Assess the morphology of the erythrocytes.
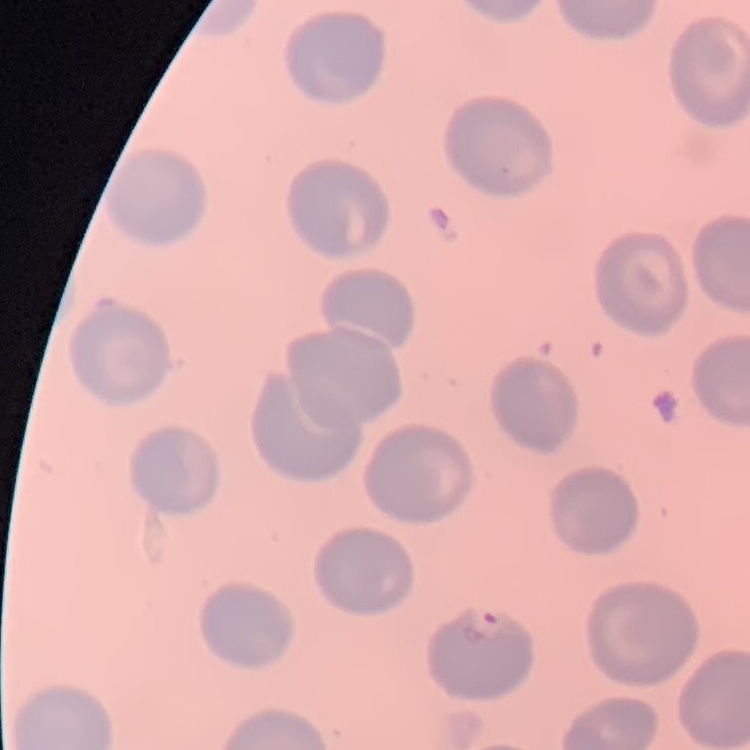

No rouleaux formation.

Stained with either Field's or Giemsa. Thin blood smear. One tile cut from a larger photomicrograph.